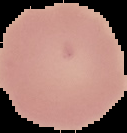
Summary:
  - Result: no malaria parasites detected
  - Image size: 127×133 pixels
  - Image type: segmented cell region on a black background
  - Preparation: thin blood film